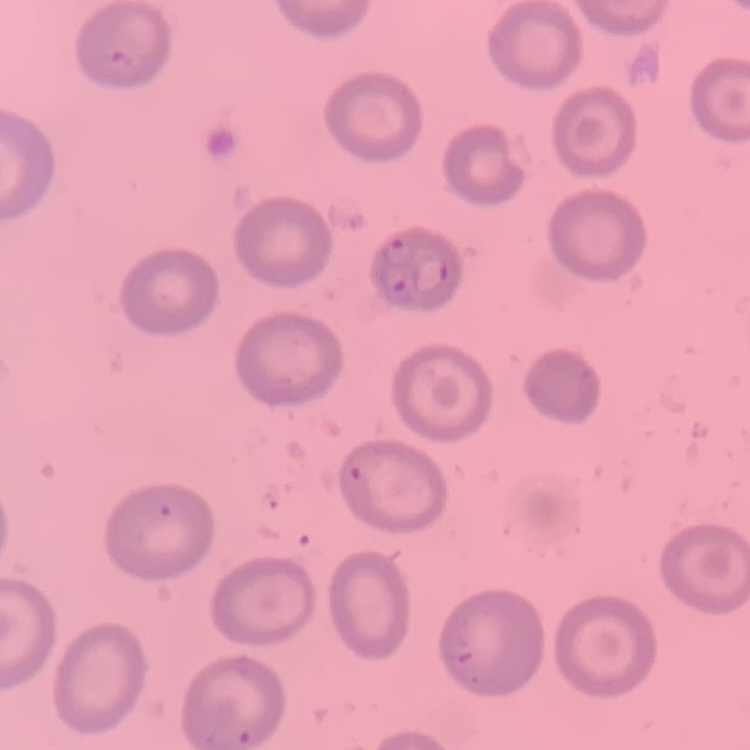
erythrocyte morphology = no rouleaux formation
stain = Field's or Giemsa
image type = square crop of a larger photomicrograph
preparation = thin blood film